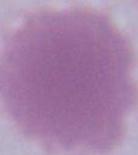

1000x magnification. An erythrocyte is seen. Photomicrograph.